Report the malaria status of this cell.
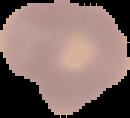
Uninfected.

{
  "image_type": "segmented cell region with the area outside set to black",
  "preparation": "thin blood film",
  "image_size": "130×118 pixels"
}